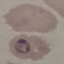
Summary:
  - Malaria status: parasitized
  - Stain: Giemsa
  - Capture: smartphone through the microscope eyepiece
  - Preparation: thin smear
  - Image type: cell patch, automatically extracted from a larger field of view and resized to 64 × 64 pixels